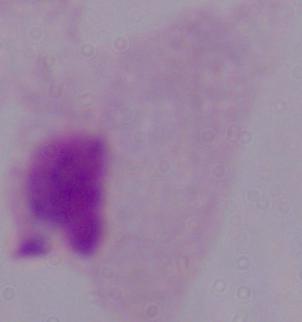
modality = photomicrograph
identification = trichomonad
magnification = 1000x